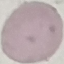
malaria status = uninfected
stain = Giemsa
image type = automatically extracted cell patch, resized to 64 × 64 pixels
capture = smartphone camera at the microscope eyepiece
preparation = thin smear